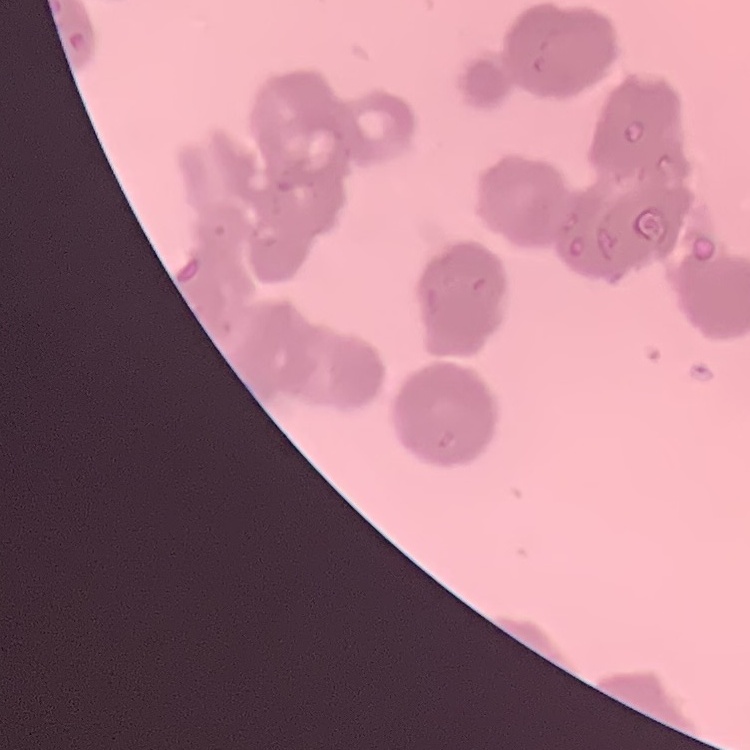
Summary:
  - Erythrocyte morphology: rouleaux formation
  - Preparation: thin peripheral smear
  - Stain: Field's or Giemsa
  - Image type: one tile cut from a larger photomicrograph